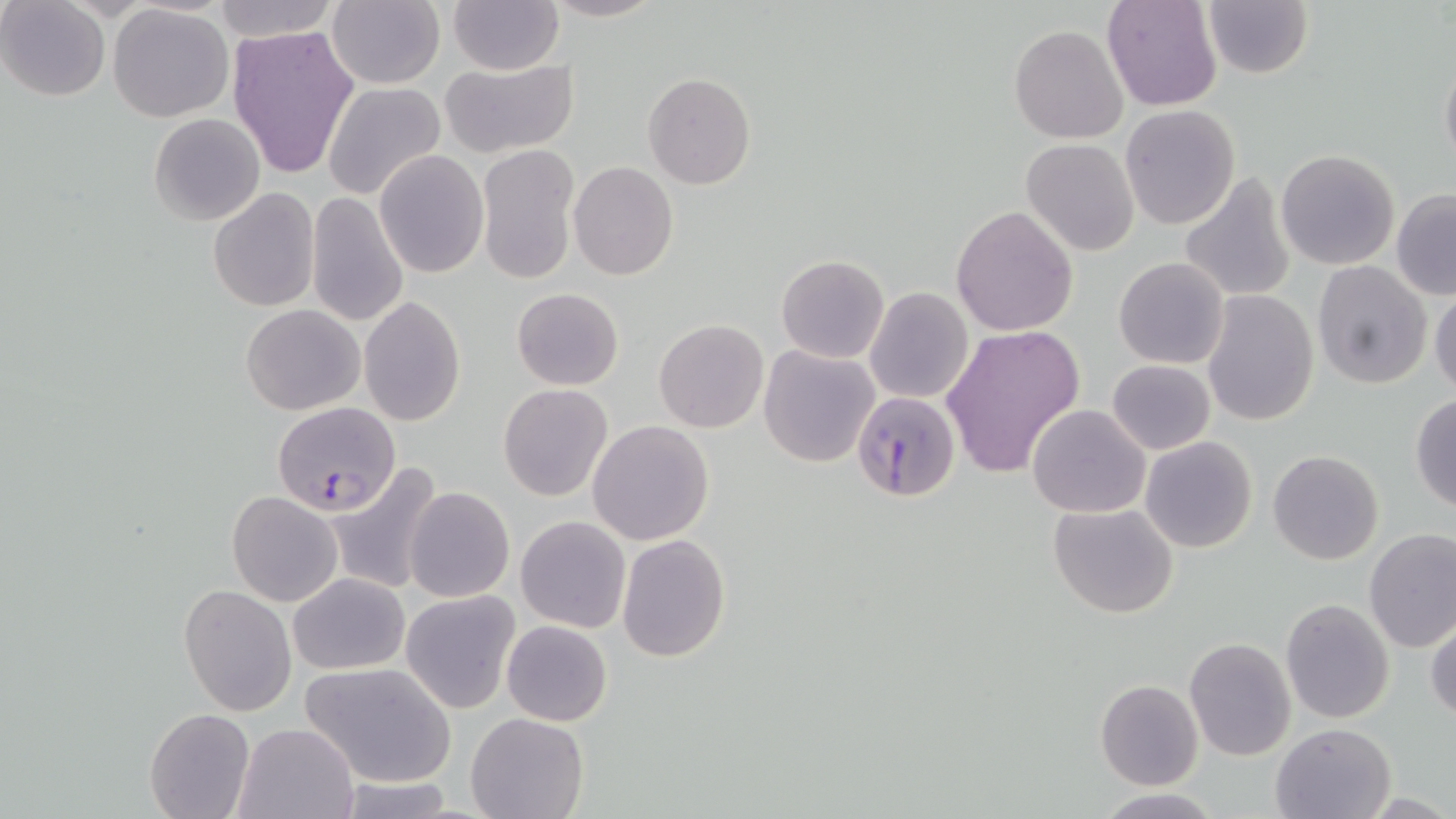

slide-level diagnosis = Plasmodium falciparum
uninfected red blood cell locations = approximate bounding boxes as (x1,y1)-(x2,y2) corner pairs in pixels: (211,0)-(339,41), (447,0)-(564,74), (543,0)-(665,22), (1101,0)-(1222,112), (0,1)-(111,100), (325,1)-(445,88), (1200,2)-(1314,79), (108,4)-(234,122), (227,24)-(359,180), (1008,24)-(1130,145), (1439,48)-(1456,178), (438,59)-(579,160), (643,73)-(756,190), (322,80)-(447,202), (1120,104)-(1240,230), (148,112)-(266,226), (1022,139)-(1139,255), (476,144)-(579,289), (1276,148)-(1401,271), (374,150)-(489,278), (568,161)-(678,281), (307,167)-(486,308), (1177,173)-(1297,305), (207,188)-(321,313), (1391,189)-(1456,300), (305,192)-(409,327), (951,205)-(1077,336), (775,254)-(889,364), (1113,258)-(1231,369), (1310,260)-(1432,388), (1429,283)-(1456,399), (511,287)-(624,389), (866,287)-(973,403), (1201,291)-(1319,426), (359,296)-(467,426), (241,305)-(366,415), (653,319)-(768,433), (940,325)-(1085,478), (759,344)-(882,467), (1107,359)-(1215,454), (498,383)-(614,501), (1410,394)-(1456,513), (1027,403)-(1151,517), (587,420)-(714,546), (1139,436)-(1258,553), (1267,450)-(1384,566), (324,463)-(445,596), (404,484)-(514,603), (226,491)-(342,606), (1048,501)-(1179,618), (515,515)-(632,635), (1363,528)-(1456,653), (617,533)-(733,662), (1314,568)-(1452,705), (287,572)-(409,675), (178,585)-(298,718), (399,590)-(521,712), (1281,597)-(1395,723), (1426,617)-(1456,724), (502,620)-(612,725), (1184,636)-(1297,761), (301,661)-(456,789), (1095,679)-(1204,790), (143,709)-(255,819), (467,713)-(588,819), (235,721)-(361,819), (1270,721)-(1396,819), (327,775)-(458,818), (1094,791)-(1223,819)
preparation = thin blood film
stain = May-Grünwald-Giemsa
Plasmodium falciparum-infected red blood cell locations = approximate bounding boxes as (x1,y1)-(x2,y2) corner pairs in pixels: (851,392)-(961,504), (270,401)-(401,516)
magnification = 1000x
image size = 1456×819 pixels
modality = light microscopy
field of view = one of a larger specimen